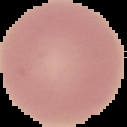
preparation = thin blood smear
image size = 127×127 pixels
malaria status = uninfected
image type = segmented cell region on a black background